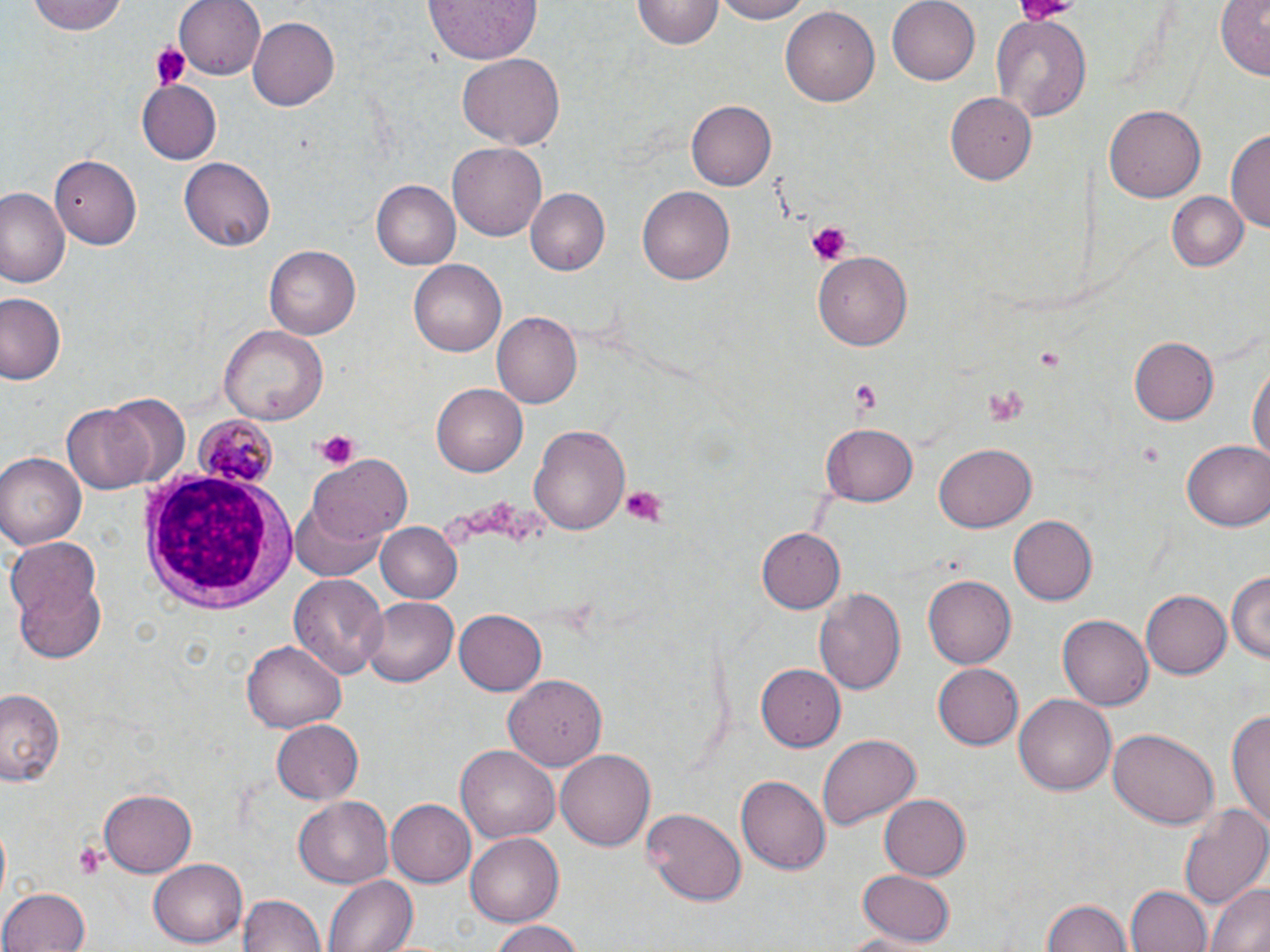

Summary:
  - Coordinate format: approximate bounding boxes as named x1/y1/x2/y2 corners in pixels
  - Plasmodium malariae-infected red blood cell locations: (x1=194, y1=413, x2=276, y2=488)
  - White blood cell locations: (x1=142, y1=470, x2=300, y2=615)
  - Uninfected red blood cell locations: (x1=30, y1=0, x2=129, y2=36), (x1=174, y1=0, x2=266, y2=79), (x1=425, y1=0, x2=541, y2=65), (x1=633, y1=0, x2=721, y2=50), (x1=710, y1=0, x2=812, y2=24), (x1=886, y1=0, x2=979, y2=85), (x1=1216, y1=1, x2=1269, y2=78), (x1=781, y1=7, x2=879, y2=107), (x1=990, y1=12, x2=1092, y2=121), (x1=247, y1=14, x2=339, y2=108), (x1=457, y1=51, x2=566, y2=151), (x1=139, y1=81, x2=221, y2=164), (x1=944, y1=91, x2=1035, y2=184), (x1=687, y1=100, x2=776, y2=191), (x1=1104, y1=104, x2=1203, y2=204), (x1=1228, y1=128, x2=1269, y2=237), (x1=448, y1=143, x2=548, y2=240), (x1=51, y1=153, x2=141, y2=249), (x1=178, y1=157, x2=276, y2=250), (x1=373, y1=181, x2=459, y2=269), (x1=0, y1=186, x2=65, y2=286), (x1=639, y1=186, x2=734, y2=285), (x1=525, y1=187, x2=609, y2=276), (x1=1165, y1=191, x2=1248, y2=271), (x1=264, y1=245, x2=361, y2=338), (x1=814, y1=248, x2=911, y2=347), (x1=409, y1=259, x2=506, y2=356), (x1=0, y1=292, x2=67, y2=386), (x1=492, y1=312, x2=583, y2=408), (x1=220, y1=325, x2=327, y2=426), (x1=1128, y1=334, x2=1220, y2=424), (x1=1247, y1=357, x2=1269, y2=477), (x1=431, y1=383, x2=528, y2=478), (x1=104, y1=392, x2=190, y2=489), (x1=60, y1=404, x2=152, y2=496), (x1=528, y1=422, x2=631, y2=534), (x1=822, y1=422, x2=918, y2=505), (x1=1182, y1=439, x2=1270, y2=531), (x1=932, y1=444, x2=1036, y2=533), (x1=0, y1=452, x2=84, y2=551), (x1=309, y1=454, x2=413, y2=547), (x1=288, y1=494, x2=392, y2=582), (x1=1009, y1=515, x2=1097, y2=606), (x1=376, y1=521, x2=463, y2=603), (x1=756, y1=528, x2=844, y2=613), (x1=4, y1=536, x2=110, y2=663), (x1=1226, y1=569, x2=1269, y2=666), (x1=289, y1=574, x2=389, y2=679), (x1=924, y1=574, x2=1018, y2=671), (x1=816, y1=587, x2=906, y2=696), (x1=1139, y1=590, x2=1229, y2=680), (x1=360, y1=596, x2=461, y2=688), (x1=454, y1=609, x2=545, y2=694), (x1=1058, y1=615, x2=1151, y2=711), (x1=242, y1=639, x2=345, y2=731), (x1=931, y1=662, x2=1024, y2=750), (x1=756, y1=663, x2=844, y2=751), (x1=504, y1=676, x2=608, y2=770), (x1=0, y1=686, x2=67, y2=786), (x1=1013, y1=693, x2=1116, y2=796), (x1=1229, y1=705, x2=1270, y2=834), (x1=270, y1=718, x2=364, y2=806), (x1=1107, y1=727, x2=1219, y2=829), (x1=817, y1=733, x2=919, y2=830), (x1=456, y1=743, x2=560, y2=843), (x1=556, y1=748, x2=659, y2=849), (x1=737, y1=775, x2=830, y2=874), (x1=99, y1=791, x2=195, y2=875), (x1=879, y1=794, x2=972, y2=882), (x1=294, y1=796, x2=393, y2=887), (x1=1179, y1=798, x2=1270, y2=911), (x1=387, y1=800, x2=475, y2=886), (x1=644, y1=807, x2=745, y2=902), (x1=465, y1=834, x2=562, y2=927), (x1=148, y1=859, x2=246, y2=947), (x1=855, y1=868, x2=958, y2=945), (x1=324, y1=875, x2=416, y2=952), (x1=1205, y1=882, x2=1270, y2=952), (x1=1125, y1=884, x2=1211, y2=952), (x1=2, y1=887, x2=91, y2=952), (x1=238, y1=890, x2=324, y2=952), (x1=1042, y1=897, x2=1134, y2=952), (x1=488, y1=920, x2=587, y2=952)
  - Platelet locations: (x1=1017, y1=0, x2=1082, y2=20), (x1=148, y1=42, x2=192, y2=91), (x1=807, y1=220, x2=851, y2=265), (x1=1034, y1=344, x2=1063, y2=370), (x1=850, y1=379, x2=886, y2=418), (x1=982, y1=383, x2=1028, y2=429), (x1=315, y1=429, x2=359, y2=469), (x1=620, y1=485, x2=666, y2=524), (x1=72, y1=840, x2=110, y2=877)
  - Slide-level diagnosis: Plasmodium malariae
  - Field of view: one of a larger specimen
  - Image size: 1270×952 pixels
  - Preparation: thin blood smear
  - Stain: May-Grünwald-Giemsa
  - Magnification: 1000x
  - Modality: light microscopy